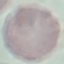

Summary:
  - Result: negative for malaria parasites
  - Stain: Giemsa
  - Preparation: thin blood smear
  - Image type: cell patch, automatically extracted from a larger field of view and resized to 64 × 64 pixels
  - Capture: smartphone through the microscope eyepiece